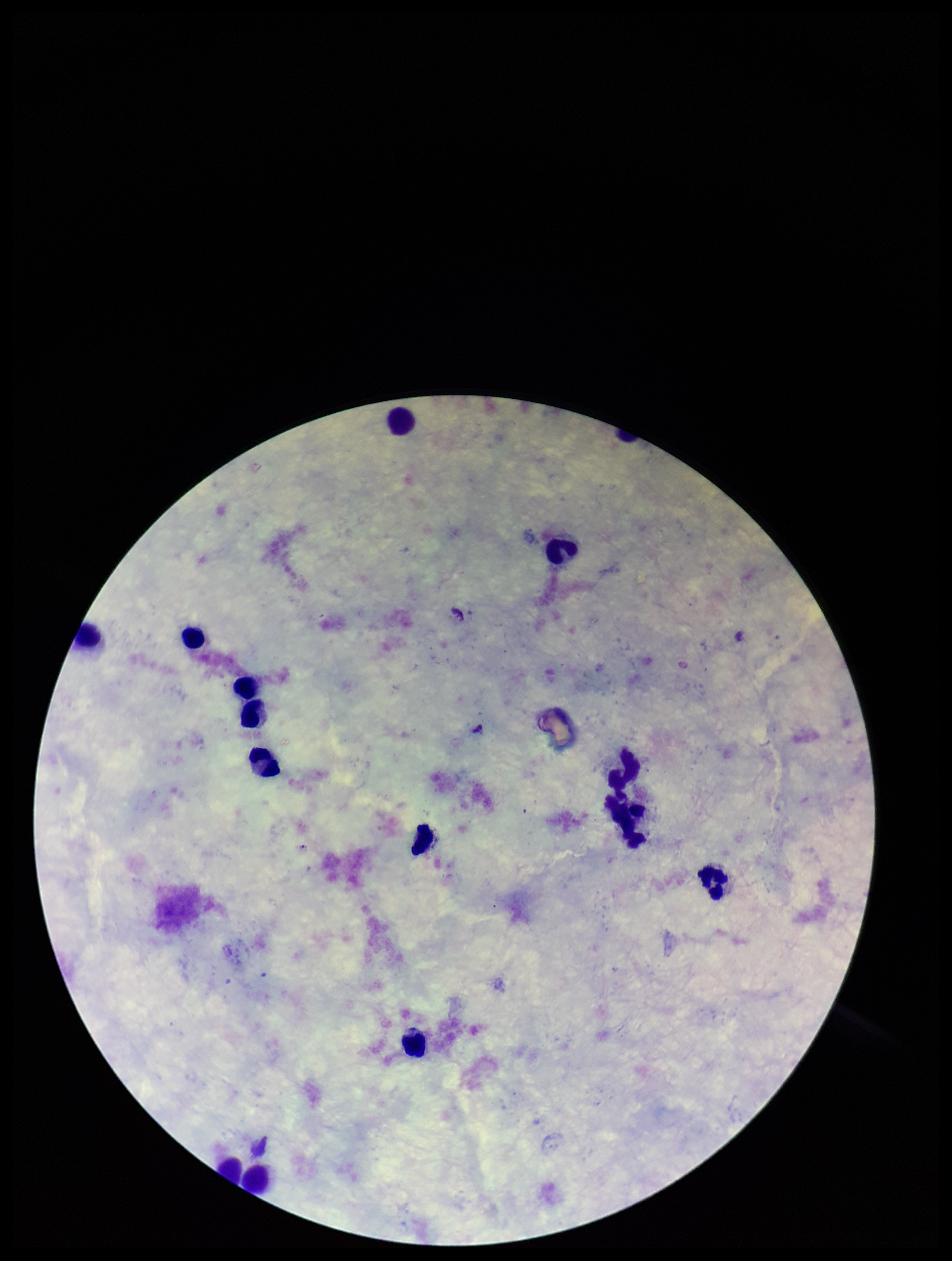
Plasmodium parasites: none identified. Patient malaria status: negative. Giemsa stain. Single field of view. Parasite count: 0. Image is 952×1261 pixels. Leukocyte count: 13. Preparation: thick smear. Smartphone photograph taken through the eyepiece of a microscope.